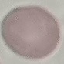

Summary:
  - Malaria status: uninfected
  - Image type: cell patch, automatically extracted from a larger field of view and resized to 64 × 64 pixels
  - Stain: Giemsa
  - Capture: smartphone through the microscope eyepiece
  - Preparation: thin smear